State which cell type is depicted.
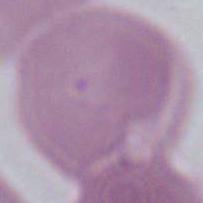
This is an erythrocyte.

Micrograph. Captured at 1000x magnification.